Assess this cell for malaria.
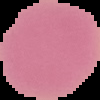
It is uninfected.

Summary:
  - Preparation: thin blood smear
  - Image size: 100×100 pixels
  - Image type: segmented cell region on a black background